Give the extent of all Plasmodium falciparum-infected red blood cells.
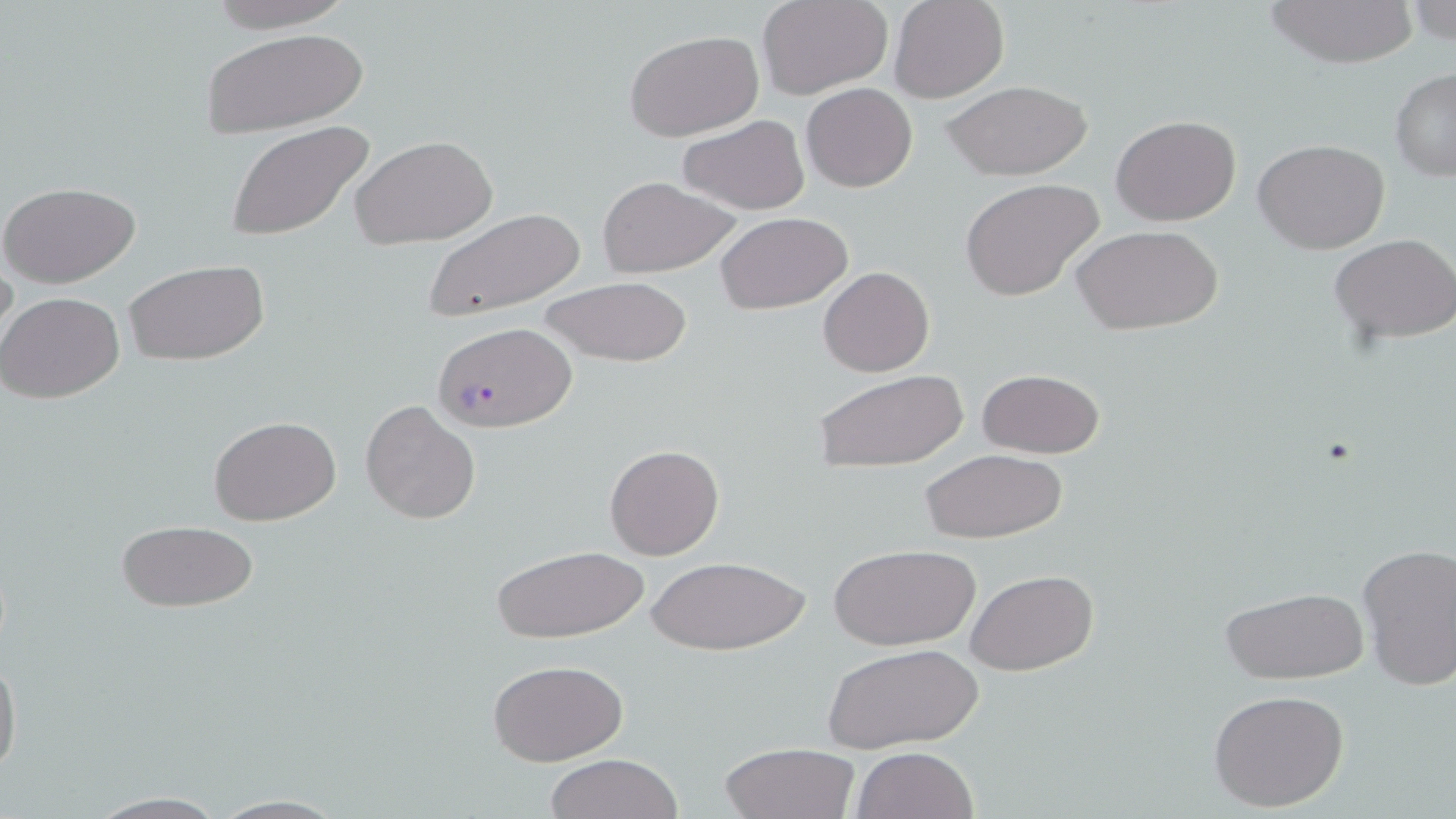

Approximate bounding boxes as [x1, y1, x2, y2] in pixels.
Plasmodium falciparum-infected red blood cells: [430, 322, 577, 432].

Uninfected red blood cell locations: [201, 0, 360, 31], [759, 0, 893, 98], [889, 0, 1008, 102], [1261, 0, 1420, 67], [1405, 0, 1456, 50], [201, 27, 370, 137], [624, 29, 765, 142], [1390, 68, 1456, 180], [941, 79, 1095, 182], [801, 83, 917, 193], [1110, 115, 1241, 224], [679, 116, 809, 215], [224, 121, 378, 245], [350, 134, 499, 249], [1254, 138, 1390, 254], [595, 176, 741, 277], [960, 178, 1105, 302], [0, 180, 141, 288], [421, 207, 589, 321], [716, 212, 853, 314], [1069, 223, 1223, 335], [1331, 234, 1454, 345], [123, 258, 270, 368], [818, 267, 933, 377], [538, 276, 692, 368], [1, 291, 125, 404], [975, 367, 1106, 458], [814, 368, 968, 474], [360, 399, 481, 526], [208, 416, 341, 525], [604, 443, 724, 560], [918, 449, 1071, 542], [115, 517, 261, 615], [828, 542, 982, 651], [1355, 543, 1456, 691], [490, 544, 650, 643], [646, 553, 810, 657], [966, 570, 1095, 675], [1220, 586, 1371, 685], [823, 642, 982, 754], [0, 651, 22, 783], [487, 659, 628, 766], [1208, 688, 1351, 812], [720, 742, 858, 819], [850, 746, 980, 819], [542, 753, 685, 819], [81, 791, 230, 818], [205, 794, 352, 817]. Slide-level diagnosis: Plasmodium falciparum. Image is 1456×819 pixels. Captured at 1000x magnification. Single field of view. Light microscopy. May-Grünwald-Giemsa-stained preparation. Thin blood smear.